Identify the blood parasite species.
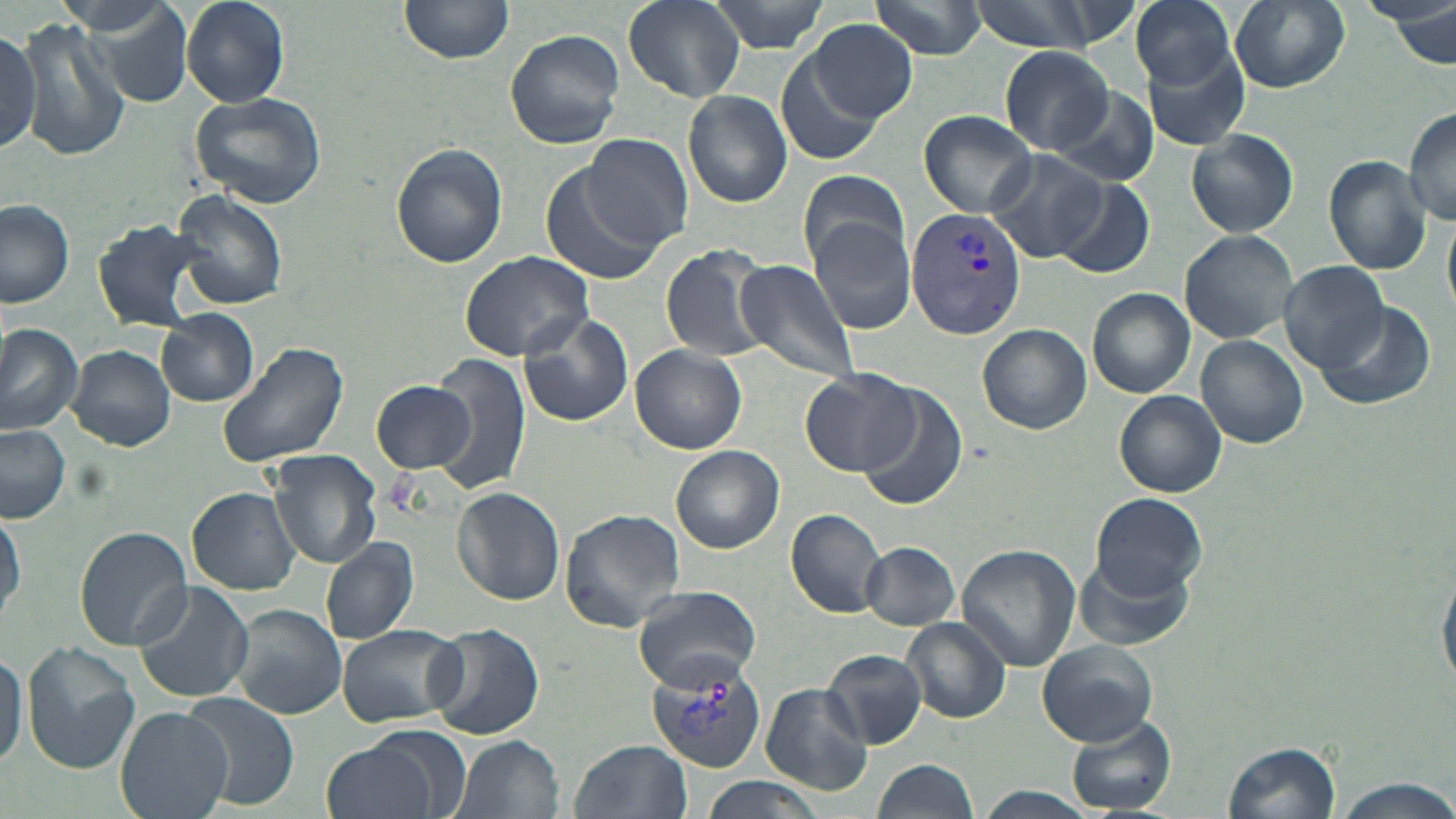
Plasmodium vivax.

Summary:
  - Coordinate format: approximate bounding boxes as [x1, y1, x2, y2] in pixels
  - Uninfected red blood cell locations: [181, 0, 290, 107], [400, 0, 515, 66], [624, 0, 745, 103], [705, 0, 833, 54], [866, 0, 989, 59], [962, 0, 1115, 54], [1130, 0, 1239, 90], [1229, 0, 1351, 92], [1364, 0, 1456, 38], [72, 3, 195, 109], [17, 17, 133, 162], [808, 18, 918, 122], [0, 25, 41, 161], [504, 29, 625, 150], [1142, 43, 1252, 152], [998, 46, 1115, 154], [777, 51, 883, 167], [1048, 82, 1161, 188], [189, 90, 327, 209], [682, 90, 792, 208], [1402, 106, 1456, 225], [920, 110, 1039, 216], [1187, 129, 1299, 237], [583, 133, 693, 248], [390, 142, 509, 269], [985, 149, 1104, 262], [1324, 156, 1431, 275], [539, 162, 666, 288], [797, 168, 909, 273], [1052, 177, 1155, 278], [172, 190, 289, 312], [0, 198, 76, 308], [808, 216, 917, 334], [90, 217, 213, 332], [1180, 230, 1298, 344], [660, 246, 773, 362], [458, 251, 594, 362], [733, 258, 861, 383], [1280, 261, 1391, 375], [1087, 288, 1194, 398], [1309, 300, 1438, 415], [155, 311, 259, 406], [518, 314, 634, 427], [977, 323, 1091, 434], [0, 324, 82, 437], [1196, 335, 1309, 449], [216, 339, 349, 470], [67, 344, 176, 452], [631, 345, 745, 454], [429, 353, 533, 496], [800, 370, 919, 475], [371, 379, 475, 476], [859, 385, 970, 512], [1114, 389, 1227, 498], [0, 423, 72, 522], [671, 444, 785, 553], [267, 449, 382, 570], [453, 487, 566, 606], [189, 488, 301, 594], [1091, 491, 1206, 596], [0, 503, 24, 626], [786, 507, 887, 616], [560, 509, 686, 631], [74, 526, 191, 649], [320, 538, 419, 645], [860, 541, 961, 629], [956, 544, 1081, 669], [1071, 552, 1193, 654], [1438, 572, 1456, 693], [131, 579, 253, 703], [633, 586, 763, 687], [226, 602, 347, 720], [901, 617, 1010, 724], [424, 621, 544, 740], [334, 623, 465, 729], [1036, 639, 1158, 747], [21, 643, 140, 773], [0, 647, 25, 772], [822, 650, 930, 748], [761, 684, 874, 795], [182, 692, 299, 809], [116, 706, 231, 819], [1064, 717, 1176, 814], [316, 732, 450, 819], [452, 734, 565, 819], [570, 737, 690, 818], [1222, 740, 1341, 819], [873, 759, 979, 818], [1337, 778, 1455, 819], [970, 786, 1101, 818]
  - Plasmodium vivax-infected red blood cell locations: [905, 209, 1026, 338], [643, 654, 767, 774]
  - Field of view: one of a larger specimen
  - Preparation: thin blood film
  - Magnification: 1000x
  - Stain: May-Grünwald-Giemsa
  - Image size: 1456×819 pixels
  - Modality: optical microscopy